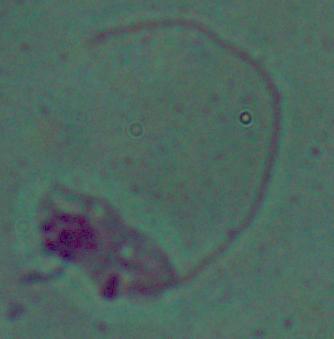

magnification: 1000x
identification: Leishmania
modality: micrograph